Identify the parasite.
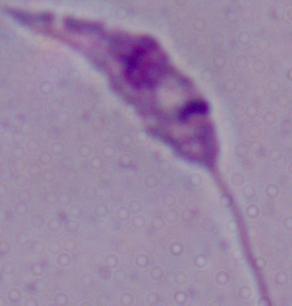

Leishmania.

Summary:
  - Magnification: 1000x
  - Modality: micrograph